Locate every blood parasite and identify its species.
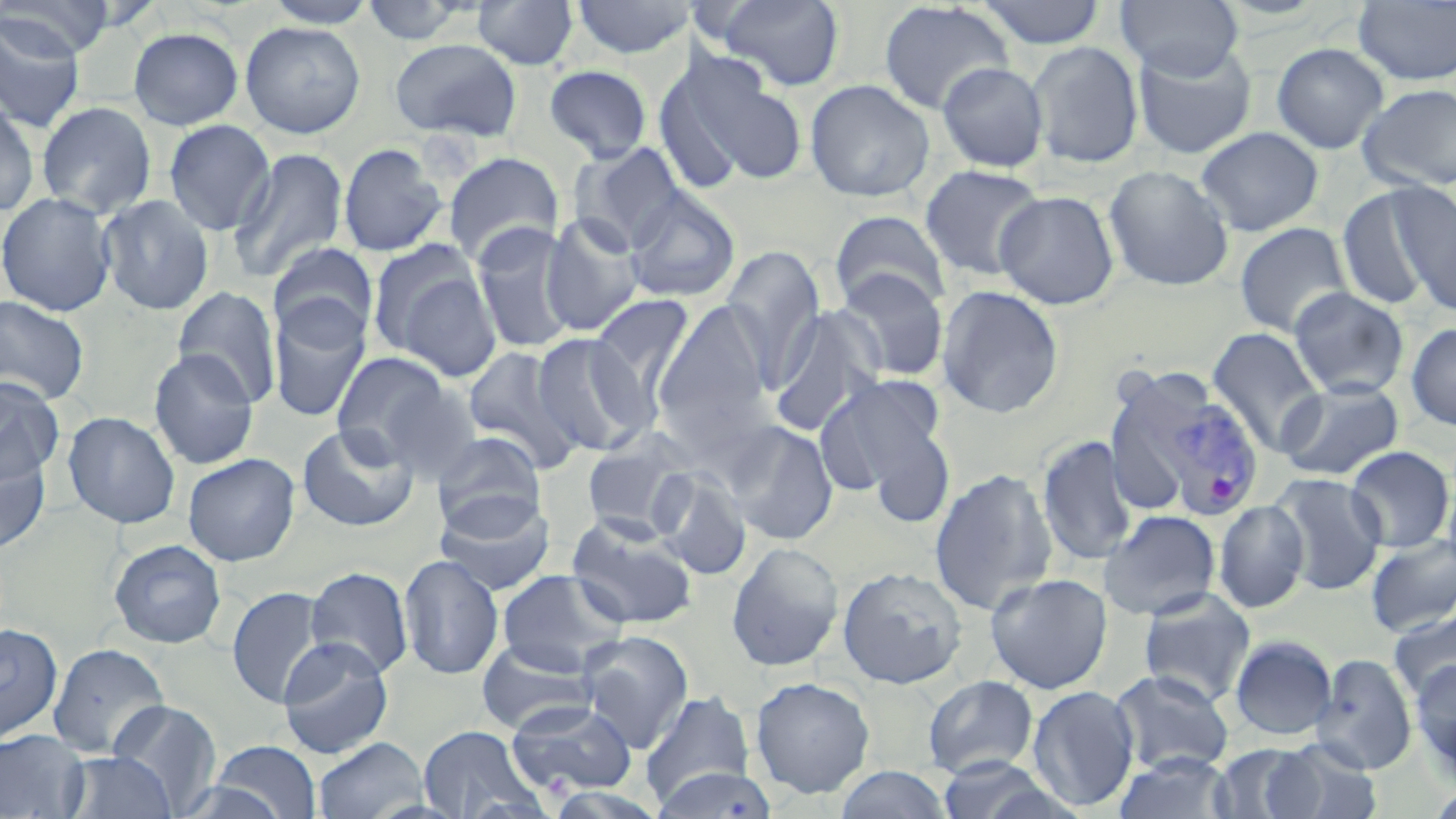

Approximate bounding boxes as (x1,y1)-(x2,y2) corner pairs in pixels.
Plasmodium vivax-infected red blood cells: (1152,389)-(1265,520).
No Plasmodium falciparum, Plasmodium ovale, Plasmodium malariae, Babesia divergens, or Trypanosoma brucei observed.

Summary:
  - Uninfected red blood cell locations: (2,0)-(115,58), (261,0)-(380,28), (358,0)-(473,45), (471,0)-(579,70), (572,0)-(691,60), (714,0)-(845,92), (976,0)-(1107,49), (1116,0)-(1243,80), (877,1)-(1014,115), (1353,1)-(1456,85), (0,13)-(86,133), (240,21)-(365,139), (128,26)-(244,130), (389,38)-(522,142), (1028,41)-(1144,168), (1132,42)-(1257,159), (1271,42)-(1389,154), (685,58)-(810,185), (936,61)-(1049,172), (544,64)-(653,163), (652,64)-(748,196), (804,78)-(935,202), (1358,83)-(1456,192), (0,100)-(41,217), (36,101)-(157,219), (163,119)-(276,236), (1195,126)-(1323,236), (569,142)-(688,251), (338,143)-(448,257), (229,147)-(349,283), (442,152)-(564,266), (919,164)-(1047,282), (1103,165)-(1234,291), (1337,184)-(1443,312), (1394,187)-(1455,319), (624,188)-(740,303), (994,190)-(1120,310), (0,192)-(117,317), (98,194)-(215,316), (829,210)-(951,314), (539,213)-(645,337), (1234,222)-(1353,338), (471,224)-(578,355), (368,239)-(499,373), (268,242)-(379,346), (721,247)-(826,384), (835,268)-(949,382), (936,285)-(1064,419), (172,286)-(282,407), (1288,287)-(1409,399), (587,293)-(697,414), (0,295)-(90,406), (268,297)-(372,423), (651,300)-(775,447), (767,305)-(887,436), (1405,323)-(1456,431), (1206,327)-(1326,456), (531,332)-(653,456), (461,345)-(583,471), (147,348)-(260,470), (331,351)-(450,460), (1103,369)-(1212,520), (818,374)-(950,503), (0,378)-(65,486), (1275,379)-(1404,481), (379,382)-(483,484), (62,411)-(181,529), (723,421)-(839,545), (297,423)-(418,532), (580,430)-(703,539), (431,432)-(547,535), (1036,435)-(1139,566), (1344,445)-(1455,552), (0,451)-(51,555), (183,452)-(300,566), (650,467)-(752,580), (929,467)-(1058,616), (1270,472)-(1387,595), (1442,477)-(1456,583), (434,492)-(555,595), (1213,499)-(1310,613), (1099,509)-(1222,621), (565,514)-(699,631), (1365,535)-(1456,636), (108,539)-(227,649), (726,541)-(845,672), (399,553)-(504,680), (837,565)-(967,689), (305,566)-(414,679), (495,568)-(629,675), (985,572)-(1113,694), (226,586)-(328,708), (1138,588)-(1256,707), (1388,610)-(1456,704), (0,623)-(63,743), (576,630)-(694,751), (1230,635)-(1338,740), (276,637)-(394,758), (476,638)-(597,736), (49,643)-(170,757), (1311,654)-(1418,774), (1410,659)-(1456,772), (1108,668)-(1235,776), (923,675)-(1039,778), (750,676)-(876,798), (1027,685)-(1140,812), (640,690)-(756,806), (505,699)-(637,798), (108,700)-(222,813), (417,724)-(543,819), (0,729)-(90,819), (312,737)-(429,819), (1267,739)-(1383,819), (210,741)-(322,818), (1211,744)-(1319,818), (61,751)-(176,818), (1113,752)-(1236,819), (933,756)-(1072,819), (833,766)-(954,818), (651,767)-(778,819), (1425,784)-(1456,819)
  - Slide-level diagnosis: Plasmodium vivax
  - Preparation: thin blood smear
  - Modality: light microscopy
  - Field of view: single
  - Image size: 1456×819 pixels
  - Stain: May-Grünwald-Giemsa
  - Magnification: 1000x